Point out each malaria parasite and each leukocyte.
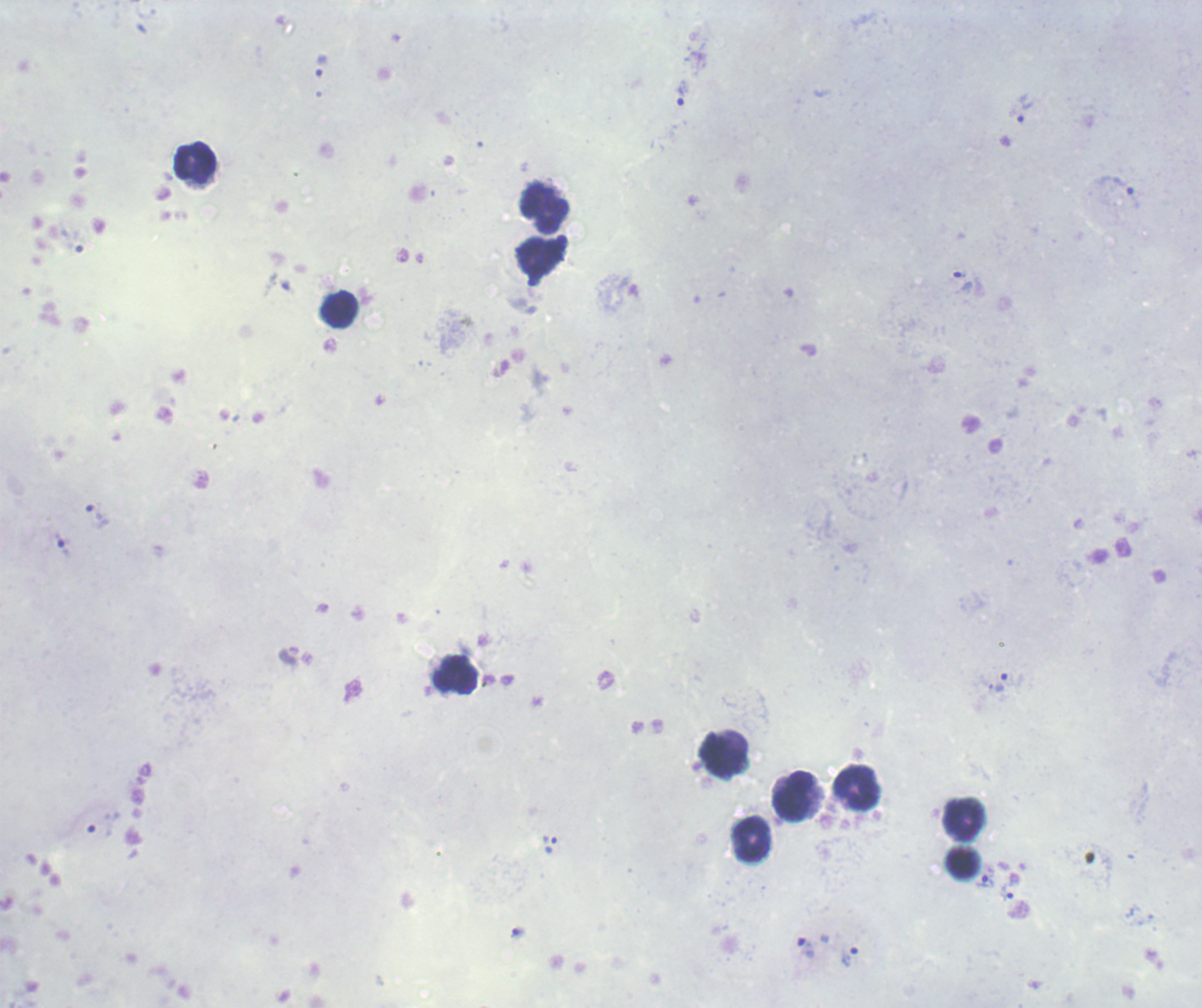

Approximate object centers, in pixels from the top-left corner.
Trophozoites: (x=320, y=66), (x=682, y=93), (x=1024, y=108), (x=1121, y=192), (x=961, y=280), (x=96, y=516), (x=63, y=545), (x=1001, y=683), (x=549, y=843), (x=985, y=882), (x=1007, y=893), (x=518, y=932), (x=806, y=947), (x=850, y=956).
No schizont or gametocyte forms observed.
Leukocytes: (x=196, y=163), (x=545, y=208), (x=338, y=309), (x=456, y=675), (x=724, y=755), (x=857, y=788), (x=794, y=795), (x=966, y=820), (x=751, y=840), (x=963, y=863).

Summary:
  - Context: previously used in an actual diagnosis
  - Magnification: 100x
  - Stain: Romanowsky
  - Preparation: thick blood film
  - Image size: 1202×1008 pixels
  - Background quality: poor
  - Field of view: one from this slide